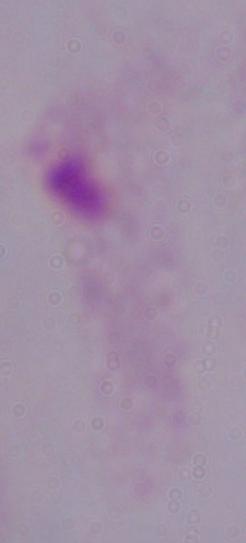

identification = trichomonad
modality = micrograph
magnification = 1000x